Assess this cell for malaria.
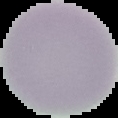

Uninfected.

Image is 118×118 pixels. Segmented cell region on a black background. From a thin blood smear.